Assess the morphology of the red blood cells.
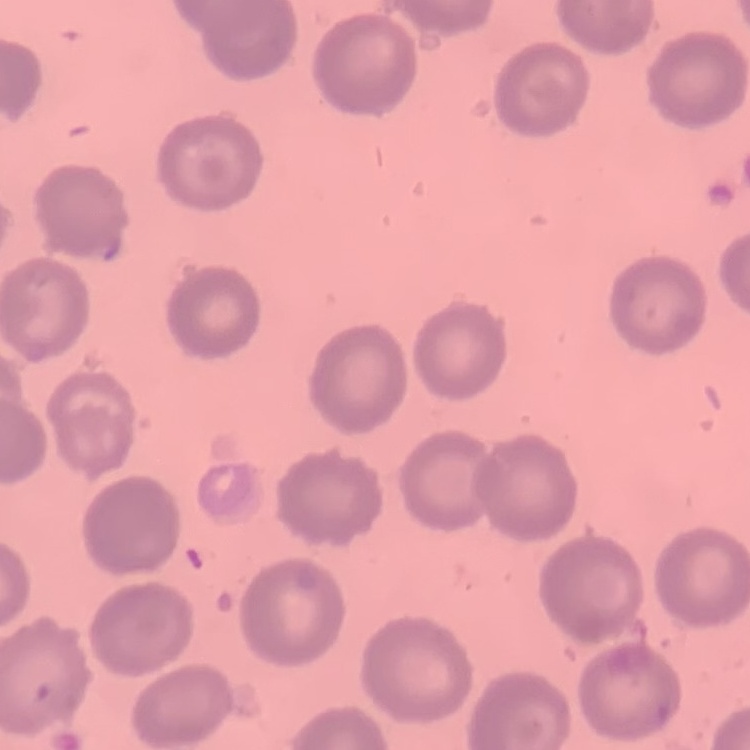

No rouleaux formation.

Square crop of a larger photomicrograph. Thin peripheral smear. Stained with either Field's or Giemsa.